Report the malaria status of this cell.
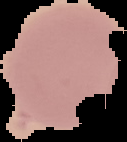

It is uninfected.

image size = 127×142 pixels
image type = segmented cell region with the area outside set to black
preparation = thin blood film